Classify this cell by malaria status.
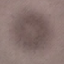

Uninfected.

Giemsa stain. Thin blood smear. Cell patch, automatically extracted from a larger field of view and resized to 64 × 64 pixels. Photographed with a smartphone camera at the microscope eyepiece.